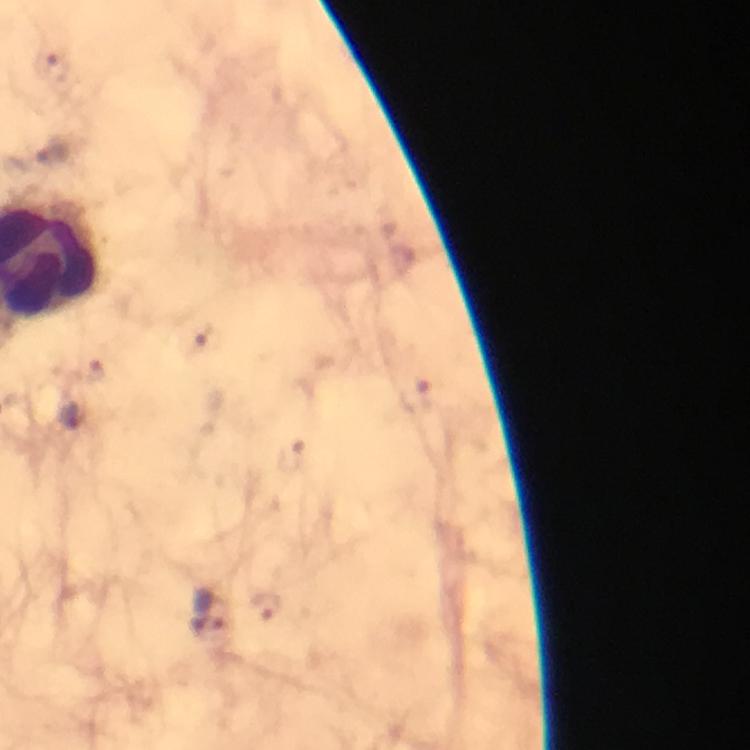
Approximate object centers, in pixels from the top-left corner. Plasmodium parasite locations: (x=212, y=613). Thick blood smear. Image is 750×750 pixels. From a malaria diagnostic workup. Photographed with a smartphone mounted on the microscope. 100x magnification. Immersion oil was used. Giemsa stain. Cropped region of a single field of view.